Give the preparation type.
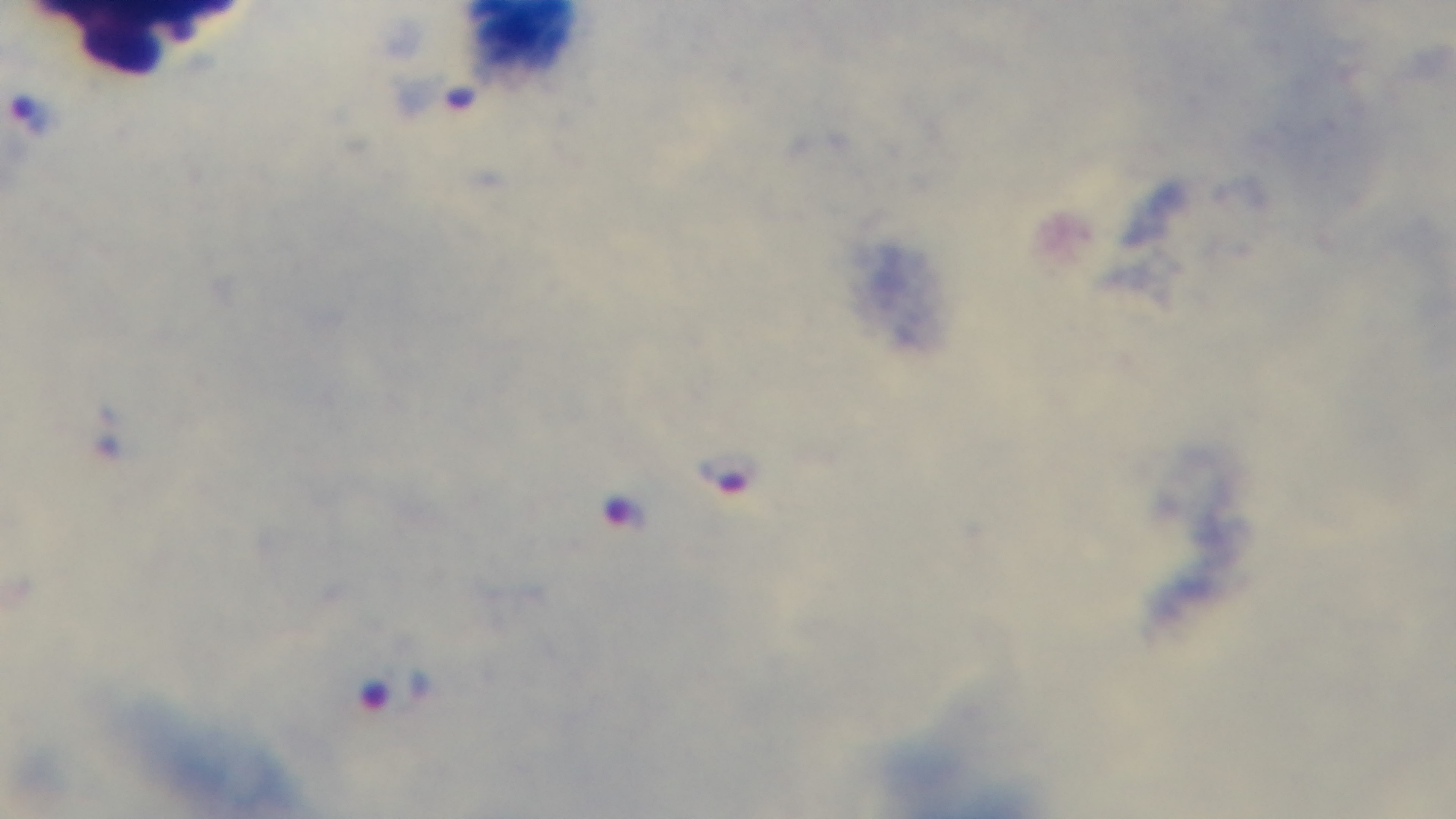
A thick smear.

field of view = single
objective = 100x oil immersion
malaria status = positive
modality = light microscopy
capture = mounted 4K digital camera
stain = Giemsa